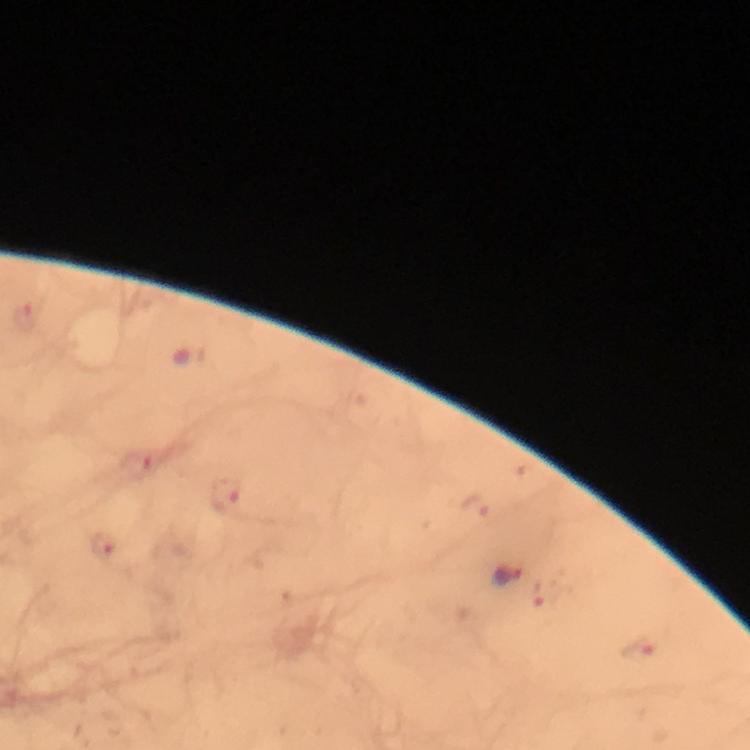
{
  "image_size": "750×750 pixels",
  "immersion_oil": "applied",
  "context": "from a malaria diagnostic workup",
  "plasmodium_parasite_locations": "approximate centers as {x, y} in pixels: {506, 575}, {638, 652}",
  "capture": "smartphone mounted on the microscope",
  "stain": "Giemsa",
  "magnification": "100x",
  "preparation": "thick blood smear",
  "cropped_from": "one field of view"
}